State which parasite is depicted.
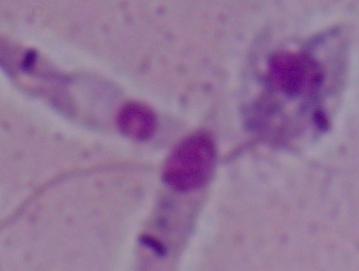

This is Leishmania.

Captured at 1000x magnification. Micrograph.